Describe the morphology of the red blood cells.
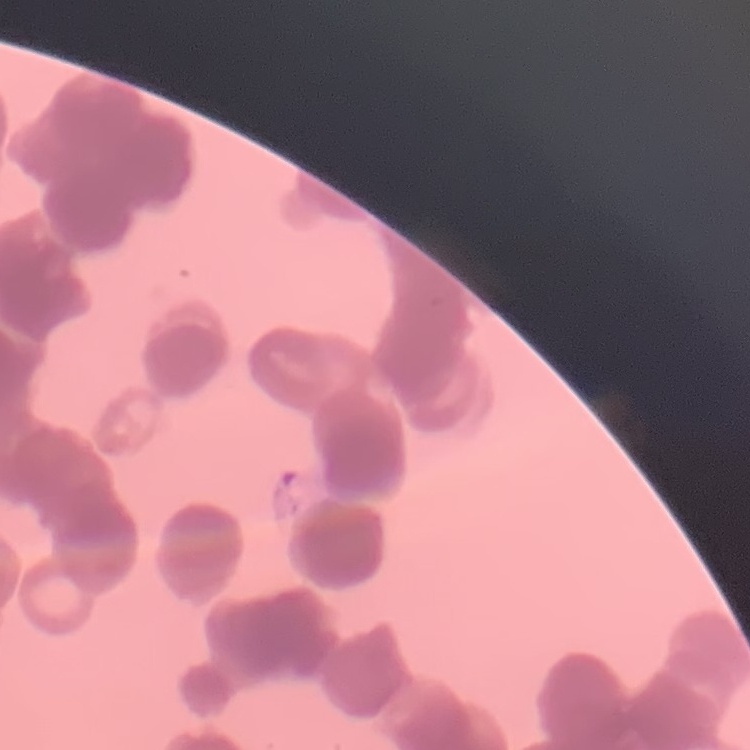

They show rouleaux formation.

{
  "image_type": "one tile cut from a larger photomicrograph",
  "stain": "Field's or Giemsa",
  "preparation": "thin blood film"
}